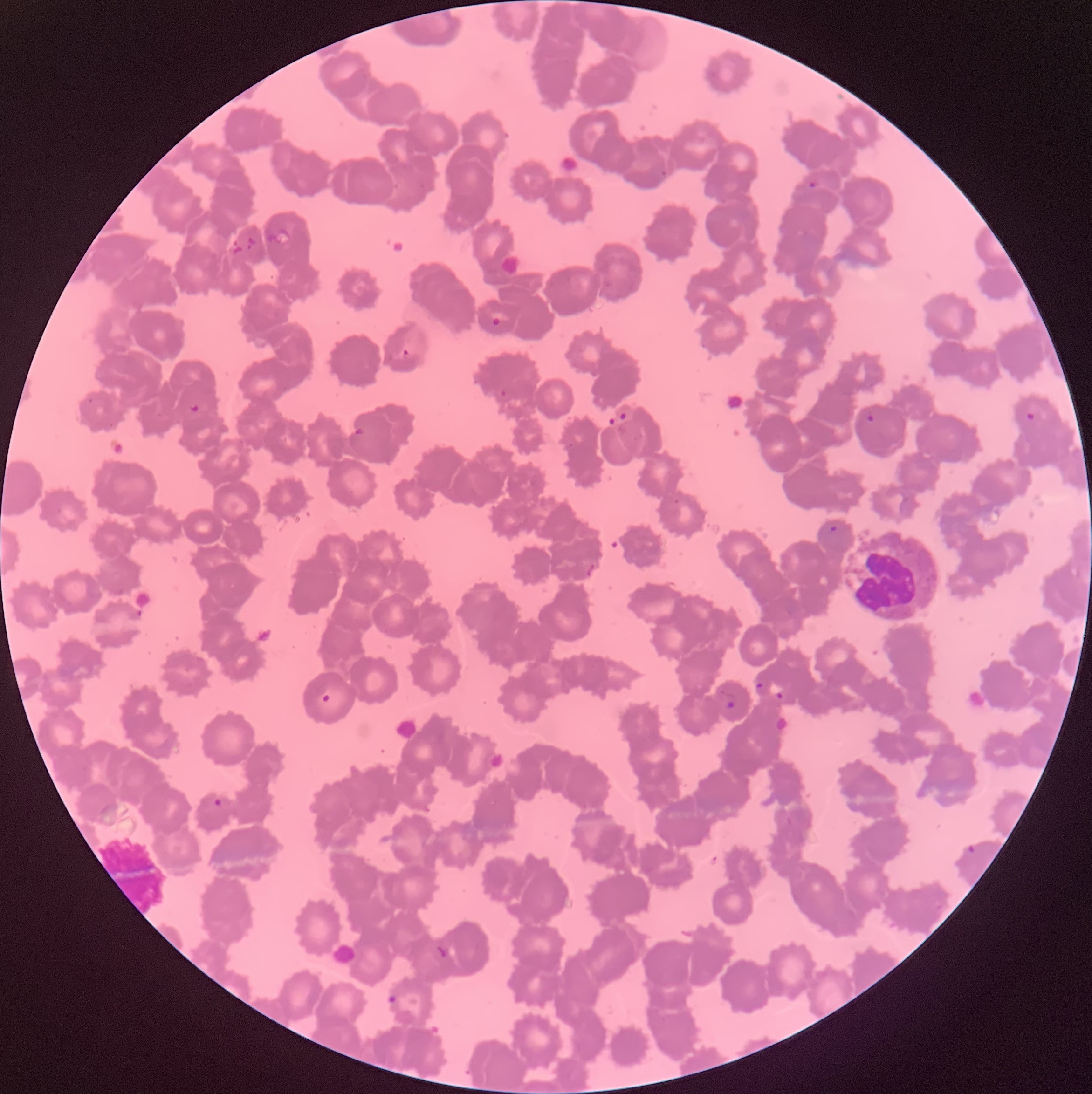
Summary:
  - Coordinate format: approximate bounding boxes as named x1/y1/x2/y2 corners in pixels
  - Plasmodium parasite locations: (x1=808, y1=177, x2=822, y2=188), (x1=491, y1=316, x2=502, y2=327), (x1=402, y1=348, x2=411, y2=360), (x1=498, y1=389, x2=506, y2=398), (x1=190, y1=402, x2=202, y2=415), (x1=1024, y1=410, x2=1039, y2=422), (x1=618, y1=411, x2=627, y2=422), (x1=866, y1=413, x2=875, y2=423), (x1=607, y1=416, x2=616, y2=427), (x1=354, y1=427, x2=365, y2=438), (x1=826, y1=524, x2=840, y2=538), (x1=753, y1=680, x2=766, y2=690), (x1=719, y1=690, x2=738, y2=710), (x1=775, y1=691, x2=784, y2=701), (x1=321, y1=693, x2=332, y2=704), (x1=213, y1=797, x2=225, y2=808), (x1=966, y1=843, x2=978, y2=854), (x1=435, y1=943, x2=453, y2=960), (x1=385, y1=993, x2=400, y2=1010)
  - White blood cell locations: (x1=847, y1=528, x2=944, y2=625)
  - Preparation: thin blood smear
  - Red blood cell morphology: rouleaux formation
  - Modality: light microscopy
  - Image size: 1092×1094 pixels